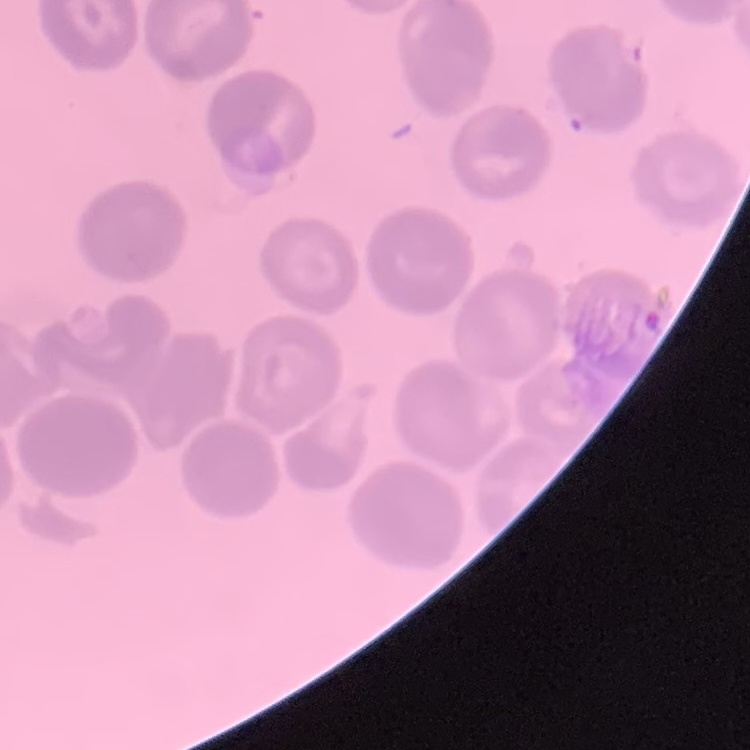 The erythrocytes exhibit no rouleaux formation. Stained with either Field's or Giemsa. Thin blood smear. One tile cut from a larger photomicrograph.